State which parasite is depicted.
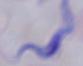

A trypanosome.

{
  "modality": "photomicrograph",
  "magnification": "1000x"
}